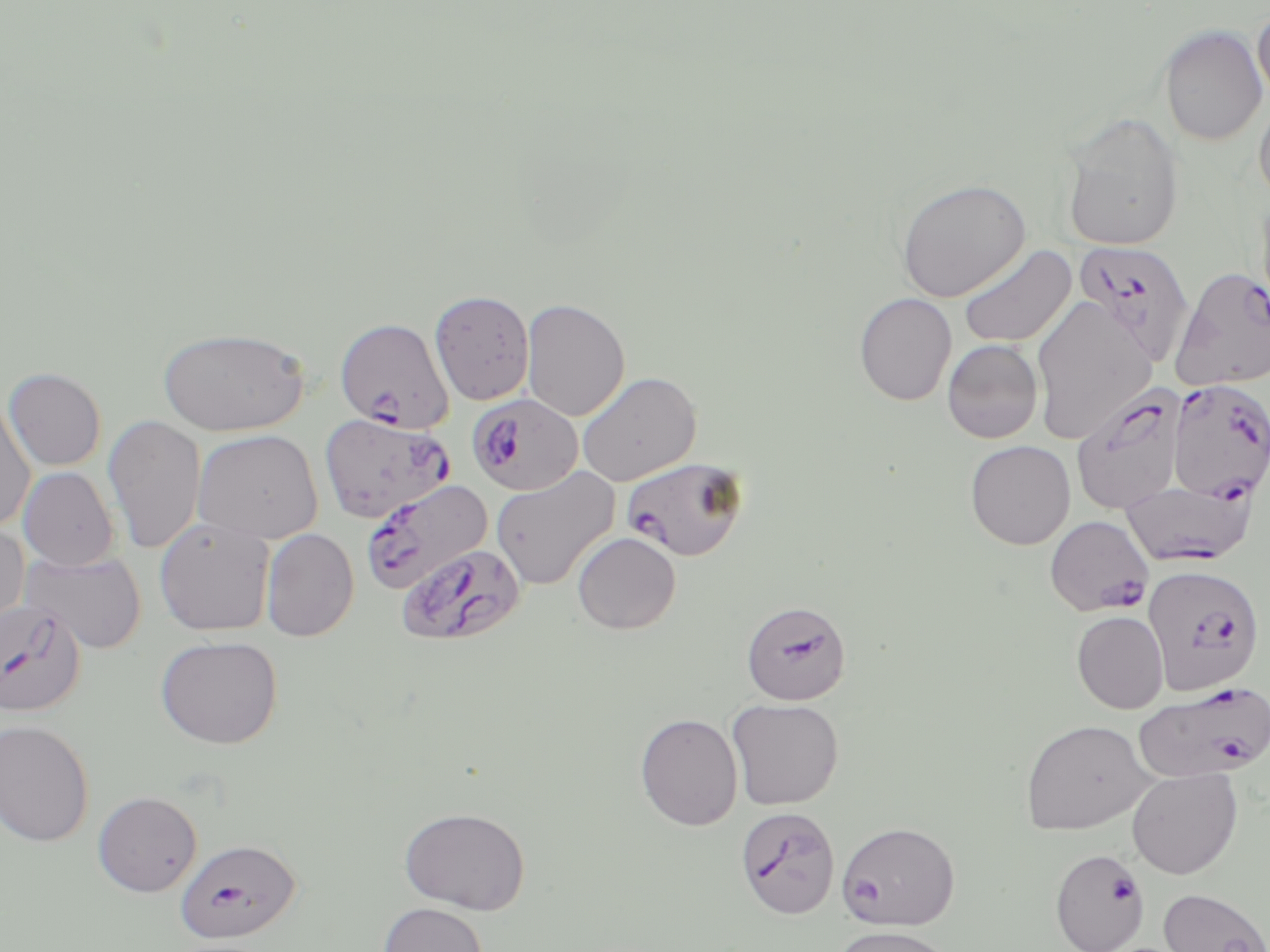
{
  "slide_level_diagnosis": "Plasmodium falciparum",
  "field_of_view": "single",
  "image_size": "1270×952 pixels",
  "plasmodium_falciparum_infected_red_blood_cell_locations_subset": "approximate bounding boxes as [x1, y1, x2, y2] in pixels: [1074, 240, 1195, 368], [1170, 268, 1270, 391], [335, 318, 453, 433], [1167, 377, 1269, 503], [1071, 383, 1188, 515], [466, 393, 583, 496], [319, 412, 455, 523], [621, 456, 749, 562], [360, 479, 493, 596], [1121, 480, 1256, 568], [1044, 514, 1154, 616], [397, 543, 526, 648], [1143, 564, 1265, 695], [0, 599, 86, 718], [741, 600, 851, 705], [1133, 681, 1270, 783], [175, 838, 300, 943], [1050, 848, 1147, 952]",
  "modality": "optical microscopy",
  "magnification": "1000x",
  "uninfected_red_blood_cell_locations_subset": "approximate bounding boxes as [x1, y1, x2, y2] in pixels: [1252, 5, 1270, 107], [1159, 25, 1268, 146], [1253, 90, 1270, 206], [1060, 111, 1185, 252], [896, 177, 1030, 303], [1255, 192, 1270, 330], [957, 244, 1076, 348], [430, 289, 535, 406], [854, 292, 957, 405], [1030, 297, 1156, 444], [521, 298, 630, 421], [157, 327, 309, 435], [942, 339, 1043, 443], [2, 366, 106, 470], [577, 371, 701, 486], [0, 396, 36, 532], [103, 415, 206, 555], [193, 429, 323, 544], [964, 440, 1076, 550], [18, 467, 119, 570], [491, 467, 619, 591], [154, 518, 276, 637], [0, 522, 30, 636], [261, 528, 359, 642], [572, 532, 681, 634], [20, 550, 146, 654], [1072, 610, 1169, 713], [155, 635, 284, 749], [726, 697, 844, 810], [635, 713, 743, 831], [0, 719, 94, 846], [1020, 719, 1154, 834], [1127, 768, 1243, 879], [92, 791, 203, 897], [399, 806, 531, 914], [836, 820, 960, 931], [1158, 887, 1270, 952], [378, 902, 488, 952], [831, 925, 957, 951]",
  "stain": "May-Grünwald-Giemsa",
  "preparation": "thin blood smear"
}